Locate and identify every blood parasite.
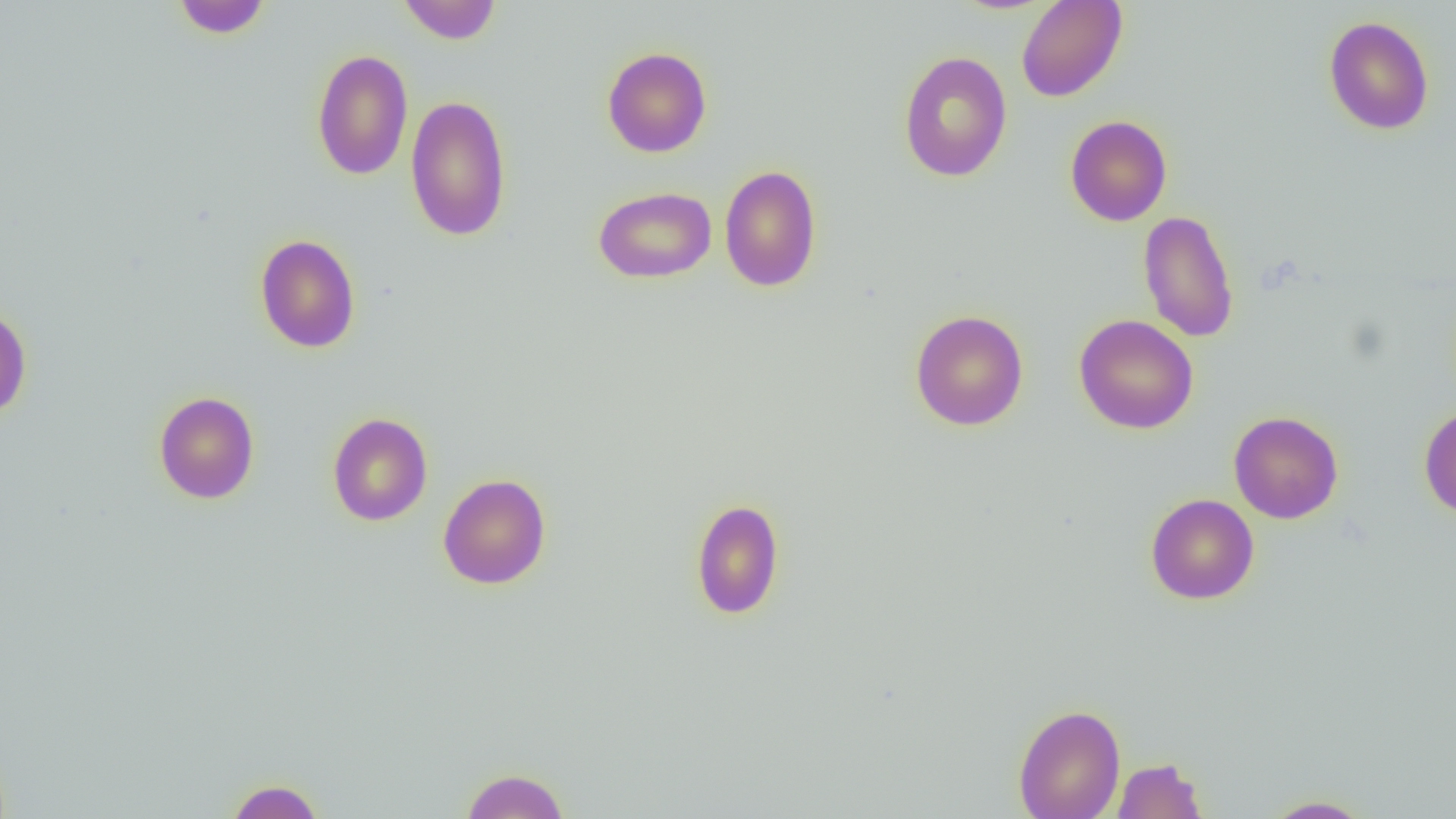

No blood parasites observed.

slide-level diagnosis = negative for blood parasites
image size = 1456×819 pixels
modality = light microscopy
preparation = thin blood smear
field of view = single
uninfected red blood cell locations = approximate bounding boxes as [x1, y1, x2, y2] in pixels: [171, 0, 272, 38], [1016, 0, 1127, 102], [396, 1, 502, 44], [1323, 15, 1434, 135], [601, 46, 712, 158], [311, 49, 413, 180], [898, 50, 1012, 183], [405, 94, 512, 242], [1065, 115, 1172, 226], [719, 164, 822, 292], [592, 185, 717, 284], [1138, 209, 1240, 343], [255, 233, 361, 353], [0, 304, 32, 421], [910, 309, 1028, 431], [1074, 314, 1198, 434], [153, 391, 259, 504], [1418, 406, 1456, 519], [1228, 411, 1344, 524], [327, 412, 433, 526], [438, 473, 551, 589], [1145, 493, 1259, 605], [690, 498, 785, 620], [1013, 703, 1125, 819], [1112, 757, 1208, 818], [460, 767, 569, 819], [224, 779, 325, 819], [1259, 795, 1376, 818]
magnification = 1000x